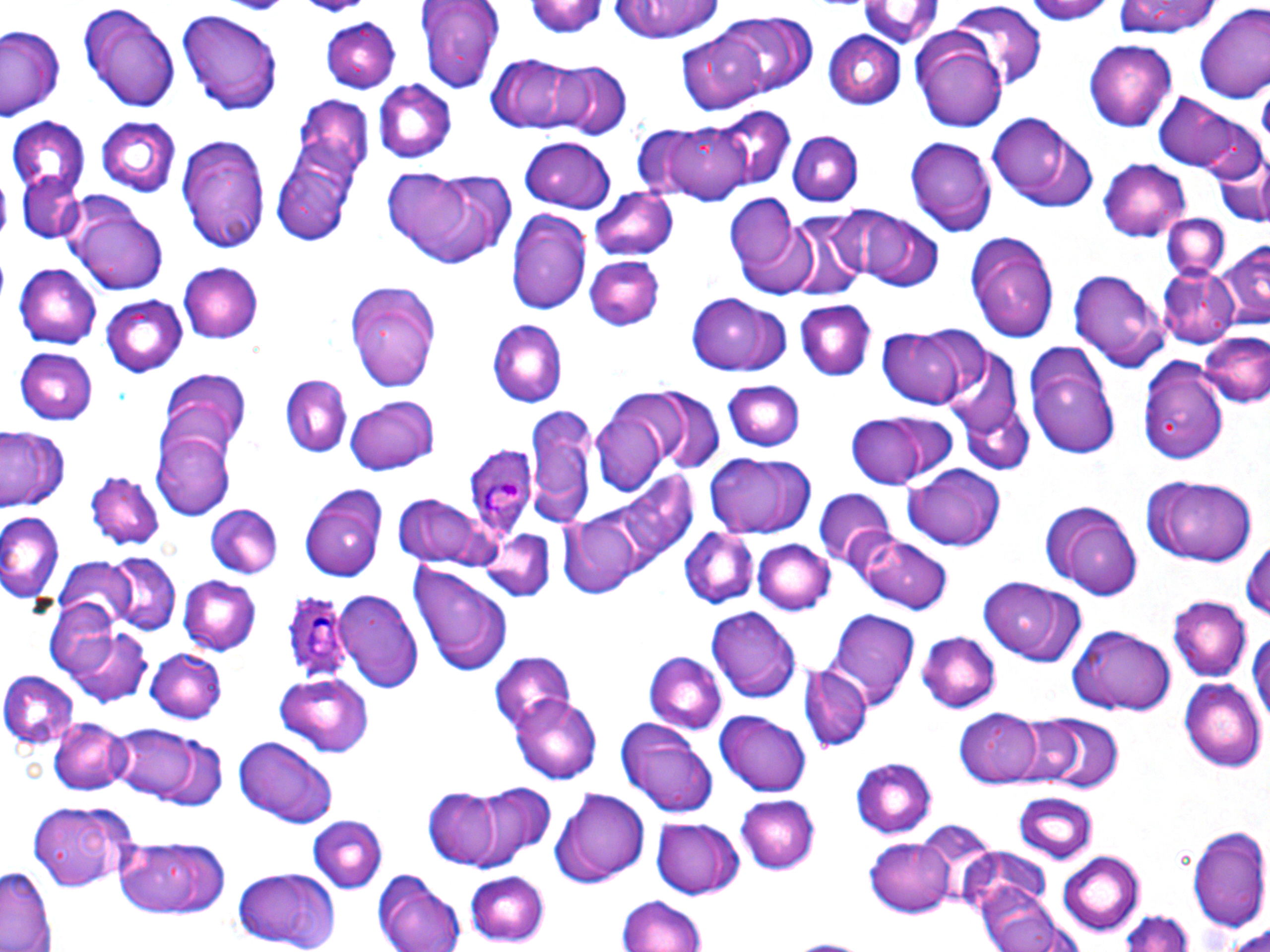

Summary:
  - Coordinate format: approximate bounding boxes as (x1,y1)-(x2,y2) corner pairs in pixels
  - Uninfected red blood cell locations: (416,0)-(505,93), (525,0)-(605,39), (608,0)-(725,43), (856,0)-(942,49), (1021,0)-(1118,23), (79,2)-(183,114), (1112,2)-(1220,39), (1196,3)-(1270,102), (180,7)-(282,112), (949,7)-(1047,87), (721,11)-(817,96), (323,17)-(399,92), (0,26)-(66,121), (910,28)-(1008,132), (677,29)-(771,113), (823,30)-(907,109), (1086,40)-(1176,130), (485,53)-(587,134), (550,61)-(629,138), (372,79)-(456,160), (1152,89)-(1257,174), (297,95)-(371,176), (715,106)-(795,186), (987,111)-(1096,209), (1193,114)-(1269,187), (8,115)-(91,204), (98,115)-(178,193), (652,120)-(753,206), (785,130)-(861,204), (177,131)-(271,254), (519,135)-(617,211), (905,136)-(995,237), (270,148)-(359,246), (1098,158)-(1190,243), (383,165)-(516,268), (1215,165)-(1268,222), (19,172)-(87,244), (589,188)-(676,262), (725,192)-(812,295), (69,197)-(169,293), (825,205)-(911,282), (508,209)-(591,317), (856,209)-(944,291), (788,212)-(868,297), (1163,213)-(1229,279), (966,233)-(1060,339), (1219,237)-(1270,326), (585,254)-(664,330), (177,261)-(265,343), (16,262)-(100,348), (1069,266)-(1169,372), (1158,266)-(1240,347), (346,278)-(440,394), (687,289)-(790,375), (103,296)-(186,378), (796,299)-(875,381), (488,318)-(569,407), (879,325)-(970,410), (1201,334)-(1269,411), (943,342)-(1030,465), (18,349)-(98,426), (1026,350)-(1122,462), (1138,354)-(1229,466), (156,367)-(249,458), (279,376)-(352,458), (722,380)-(806,452), (652,392)-(723,473), (346,396)-(438,475), (589,397)-(677,494), (954,398)-(1035,478), (528,405)-(600,525), (846,412)-(938,488), (2,429)-(68,512), (155,432)-(234,516), (705,453)-(817,538), (904,462)-(1007,551), (84,470)-(164,552), (593,471)-(698,580), (1140,474)-(1261,567), (300,482)-(386,582), (814,489)-(895,569), (394,495)-(498,571), (1042,500)-(1141,600), (205,504)-(285,579), (0,510)-(64,602), (558,513)-(641,599), (680,525)-(758,610), (475,529)-(554,603), (855,530)-(954,614), (1245,537)-(1270,626), (753,539)-(834,615), (101,554)-(181,634), (52,559)-(139,631), (411,565)-(515,676), (178,575)-(258,653), (977,578)-(1088,668), (335,590)-(424,692), (45,597)-(129,681), (1169,597)-(1249,682), (707,608)-(800,705), (829,609)-(919,709), (1070,623)-(1176,714), (1248,624)-(1270,734), (64,625)-(151,707), (917,631)-(1001,713), (148,648)-(225,723), (487,651)-(575,730), (646,652)-(728,731), (802,665)-(870,753), (1,668)-(80,747), (275,674)-(374,757), (1182,678)-(1266,770), (513,692)-(601,782), (717,708)-(814,796), (956,708)-(1044,788), (1039,713)-(1122,791), (1004,714)-(1086,786), (49,716)-(128,795), (615,718)-(720,816), (106,721)-(222,808), (231,736)-(339,829), (851,758)-(937,838), (472,784)-(553,861), (549,786)-(649,886), (425,791)-(500,869), (1012,793)-(1097,866), (736,797)-(818,872), (28,803)-(131,891), (307,815)-(386,890), (652,817)-(745,897), (916,821)-(1000,907), (1186,824)-(1270,933), (116,836)-(230,918), (867,836)-(956,917), (963,849)-(1060,938), (1058,852)-(1144,934), (1,862)-(59,952), (231,867)-(342,950), (465,871)-(550,946), (375,875)-(469,952), (975,884)-(1072,952), (618,897)-(708,952), (1116,908)-(1193,952), (1220,926)-(1270,951)
  - Plasmodium ovale-infected red blood cell locations: (462,439)-(537,535), (281,592)-(355,684)
  - Platelet locations: (234,0)-(283,16), (301,0)-(364,17)
  - Slide-level diagnosis: Plasmodium ovale
  - Magnification: 1000x
  - Image size: 1270×952 pixels
  - Field of view: single
  - Preparation: thin blood smear
  - Modality: light microscopy
  - Stain: May-Grünwald-Giemsa